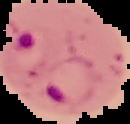

Segmented cell region on a black background. From a thin blood film. Image is 130×124 pixels. Result: Plasmodium parasites detected.